Report the malaria status of this cell.
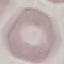

Uninfected.

Summary:
  - Capture: smartphone camera at the microscope eyepiece
  - Preparation: thin smear
  - Stain: Giemsa
  - Image type: cell patch, automatically extracted from a larger field of view and resized to 64 × 64 pixels